Locate every blood parasite and identify its species.
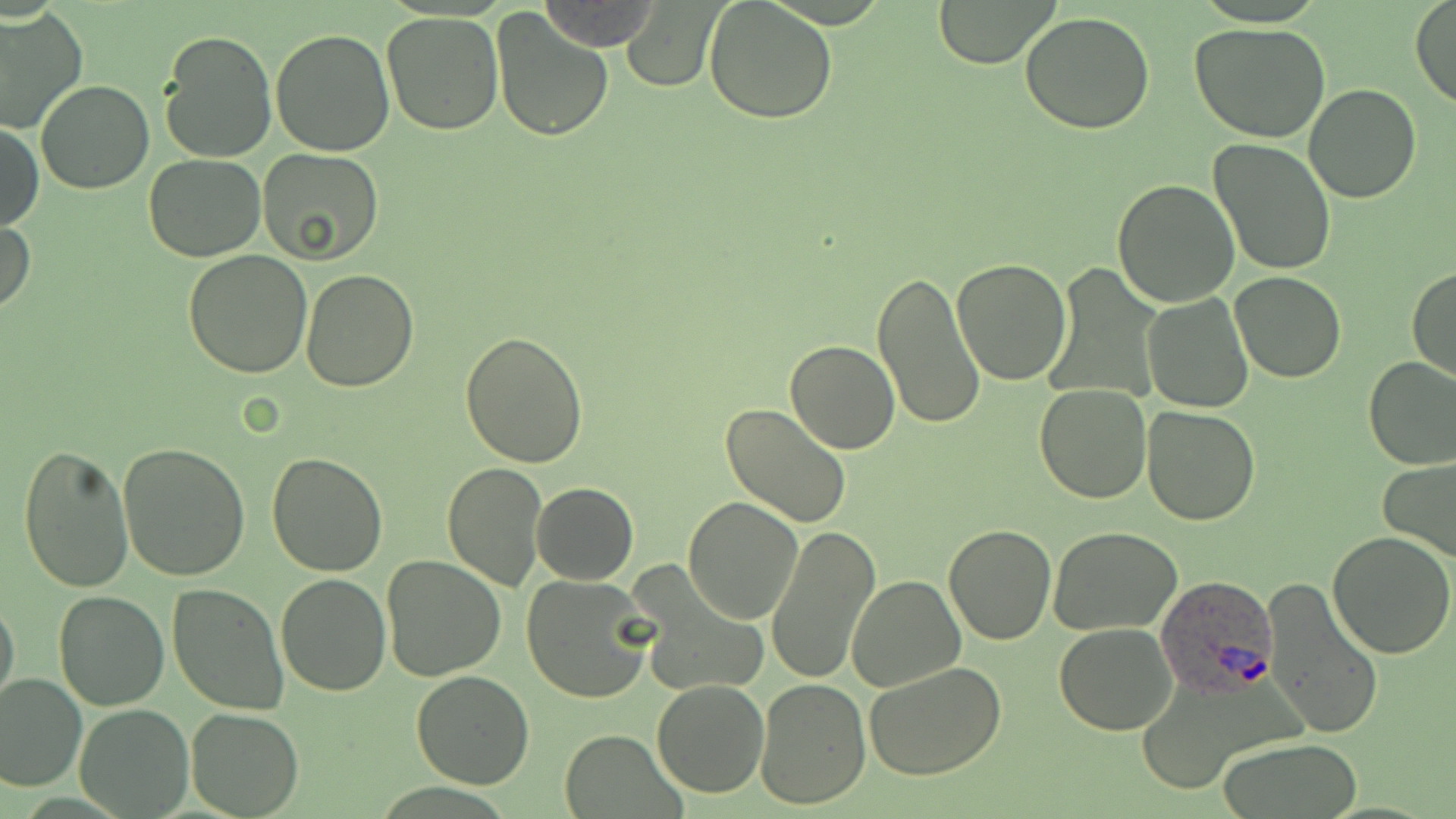

Approximate bounding boxes as (x1,y1)-(x2,y2) corner pairs in pixels.
Plasmodium ovale-infected red blood cells: (1154,574)-(1279,697).
No Plasmodium falciparum, Plasmodium malariae, Plasmodium vivax, Babesia divergens, or Trypanosoma brucei observed.

Uninfected red blood cell locations: (933,0)-(1059,67), (1410,0)-(1456,109), (703,1)-(839,122), (540,2)-(660,50), (622,2)-(722,90), (0,8)-(86,133), (491,8)-(615,142), (380,11)-(506,135), (1019,13)-(1155,134), (1189,23)-(1330,142), (270,28)-(396,157), (157,30)-(277,164), (35,80)-(154,194), (1304,83)-(1421,202), (1,122)-(43,233), (1208,138)-(1337,276), (257,147)-(384,263), (143,154)-(265,262), (1113,177)-(1240,306), (0,214)-(35,317), (183,249)-(313,377), (952,259)-(1072,387), (1406,265)-(1456,383), (300,269)-(418,392), (872,270)-(984,431), (1231,271)-(1345,383), (1142,293)-(1254,414), (801,313)-(968,448), (460,331)-(589,467), (786,340)-(898,454), (1363,356)-(1456,471), (1034,383)-(1152,504), (720,403)-(853,529), (1141,406)-(1260,526), (118,442)-(252,580), (18,444)-(134,593), (265,452)-(389,577), (1379,457)-(1456,562), (442,460)-(549,591), (532,482)-(638,584), (682,496)-(802,625), (766,524)-(879,686), (943,524)-(1057,645), (1049,526)-(1181,637), (1328,532)-(1456,660), (392,552)-(519,791), (382,556)-(505,680), (276,571)-(391,695), (521,574)-(656,704), (845,576)-(965,692), (1262,579)-(1385,742), (167,583)-(289,717), (56,589)-(169,710), (0,596)-(20,711), (1054,621)-(1178,735), (864,662)-(1009,782), (410,671)-(535,789), (0,672)-(86,791), (755,678)-(870,808), (652,679)-(769,799), (0,688)-(170,803), (75,704)-(193,817), (186,707)-(304,818), (558,730)-(684,816), (1217,737)-(1363,817). Slide-level diagnosis: Plasmodium ovale. May-Grünwald-Giemsa-stained preparation. Single field of view. Image is 1456×819 pixels. Thin blood film. Optical microscopy. Captured at 1000x magnification.